Locate every blood parasite and identify its species.
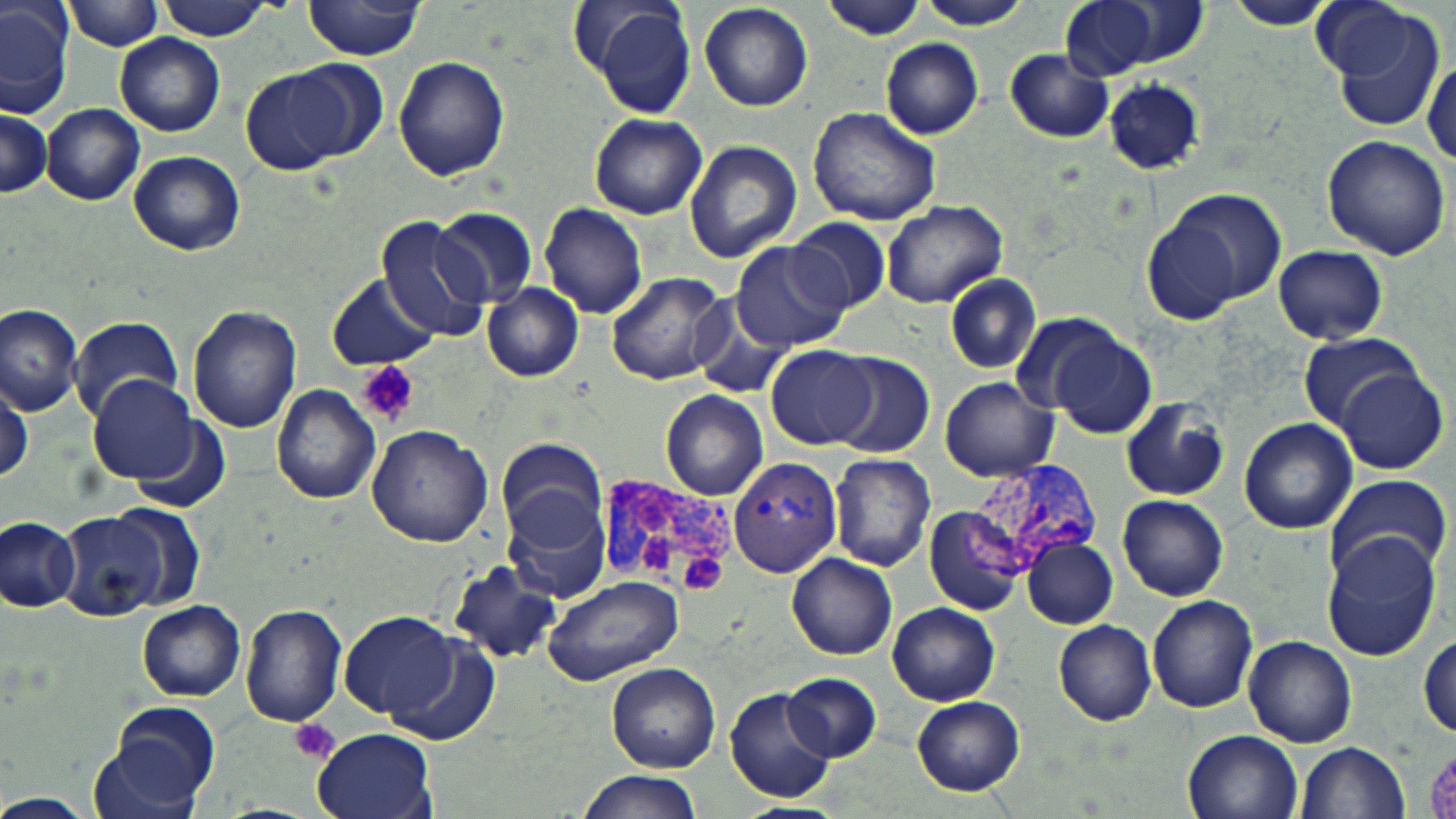

Approximate bounding boxes as named x1/y1/x2/y2 corners in pixels.
Plasmodium vivax-infected red blood cells: (x1=729, y1=455, x2=845, y2=576), (x1=969, y1=456, x2=1107, y2=571), (x1=591, y1=476, x2=733, y2=604).
No Plasmodium falciparum, Plasmodium ovale, Plasmodium malariae, Babesia divergens, or Trypanosoma brucei observed.

Summary:
  - Uninfected red blood cell locations: (x1=1, y1=0, x2=74, y2=119), (x1=913, y1=0, x2=1033, y2=29), (x1=1059, y1=0, x2=1192, y2=81), (x1=157, y1=1, x2=273, y2=39), (x1=573, y1=1, x2=696, y2=115), (x1=1225, y1=1, x2=1339, y2=32), (x1=1308, y1=1, x2=1423, y2=86), (x1=302, y1=2, x2=427, y2=60), (x1=820, y1=2, x2=927, y2=40), (x1=66, y1=3, x2=166, y2=51), (x1=699, y1=3, x2=813, y2=111), (x1=1324, y1=7, x2=1448, y2=134), (x1=116, y1=34, x2=225, y2=137), (x1=881, y1=39, x2=983, y2=140), (x1=1002, y1=48, x2=1115, y2=143), (x1=284, y1=57, x2=389, y2=160), (x1=394, y1=57, x2=510, y2=182), (x1=1421, y1=57, x2=1454, y2=175), (x1=242, y1=67, x2=350, y2=174), (x1=1102, y1=78, x2=1207, y2=176), (x1=43, y1=104, x2=145, y2=205), (x1=0, y1=106, x2=50, y2=199), (x1=808, y1=106, x2=942, y2=227), (x1=589, y1=112, x2=708, y2=219), (x1=1321, y1=135, x2=1451, y2=261), (x1=684, y1=139, x2=801, y2=262), (x1=127, y1=150, x2=245, y2=255), (x1=1153, y1=188, x2=1287, y2=315), (x1=878, y1=200, x2=1007, y2=309), (x1=539, y1=202, x2=647, y2=320), (x1=432, y1=207, x2=538, y2=309), (x1=375, y1=217, x2=488, y2=340), (x1=789, y1=217, x2=893, y2=314), (x1=730, y1=240, x2=850, y2=351), (x1=1272, y1=245, x2=1389, y2=344), (x1=606, y1=271, x2=731, y2=385), (x1=944, y1=272, x2=1041, y2=374), (x1=327, y1=274, x2=436, y2=369), (x1=482, y1=284, x2=583, y2=381), (x1=688, y1=293, x2=795, y2=400), (x1=0, y1=303, x2=84, y2=412), (x1=188, y1=303, x2=303, y2=432), (x1=1008, y1=309, x2=1126, y2=421), (x1=72, y1=316, x2=184, y2=420), (x1=1046, y1=327, x2=1159, y2=440), (x1=1296, y1=334, x2=1427, y2=432), (x1=767, y1=344, x2=877, y2=449), (x1=829, y1=353, x2=936, y2=459), (x1=1334, y1=368, x2=1449, y2=475), (x1=89, y1=376, x2=198, y2=483), (x1=0, y1=378, x2=30, y2=481), (x1=940, y1=379, x2=1059, y2=481), (x1=270, y1=383, x2=382, y2=504), (x1=660, y1=389, x2=769, y2=501), (x1=1119, y1=399, x2=1232, y2=501), (x1=1239, y1=417, x2=1358, y2=535), (x1=366, y1=425, x2=493, y2=549), (x1=496, y1=435, x2=608, y2=544), (x1=828, y1=453, x2=938, y2=571), (x1=1322, y1=474, x2=1453, y2=585), (x1=1117, y1=494, x2=1229, y2=600), (x1=504, y1=496, x2=611, y2=605), (x1=100, y1=505, x2=208, y2=614), (x1=924, y1=506, x2=1028, y2=616), (x1=59, y1=511, x2=170, y2=620), (x1=0, y1=517, x2=81, y2=614), (x1=474, y1=518, x2=594, y2=641), (x1=1321, y1=534, x2=1442, y2=662), (x1=1021, y1=538, x2=1119, y2=629), (x1=787, y1=552, x2=898, y2=659), (x1=447, y1=561, x2=560, y2=665), (x1=543, y1=574, x2=684, y2=686), (x1=1147, y1=595, x2=1260, y2=713), (x1=138, y1=601, x2=246, y2=702), (x1=240, y1=602, x2=347, y2=728), (x1=888, y1=602, x2=999, y2=705), (x1=338, y1=610, x2=459, y2=719), (x1=1053, y1=619, x2=1157, y2=725), (x1=1418, y1=630, x2=1455, y2=738), (x1=377, y1=633, x2=503, y2=747), (x1=1244, y1=636, x2=1356, y2=747), (x1=608, y1=662, x2=720, y2=772), (x1=780, y1=672, x2=882, y2=761), (x1=726, y1=686, x2=835, y2=803), (x1=912, y1=695, x2=1026, y2=796), (x1=94, y1=701, x2=223, y2=817), (x1=311, y1=728, x2=436, y2=819), (x1=1181, y1=730, x2=1302, y2=819), (x1=1296, y1=742, x2=1409, y2=819), (x1=576, y1=770, x2=701, y2=819), (x1=0, y1=794, x2=95, y2=819), (x1=733, y1=803, x2=845, y2=819)
  - Platelet locations: (x1=358, y1=361, x2=419, y2=426), (x1=682, y1=550, x2=728, y2=592), (x1=291, y1=718, x2=340, y2=765)
  - Slide-level diagnosis: Plasmodium vivax
  - Modality: light microscopy
  - Image size: 1456×819 pixels
  - Field of view: single
  - Preparation: thin blood film
  - Magnification: 1000x
  - Stain: May-Grünwald-Giemsa